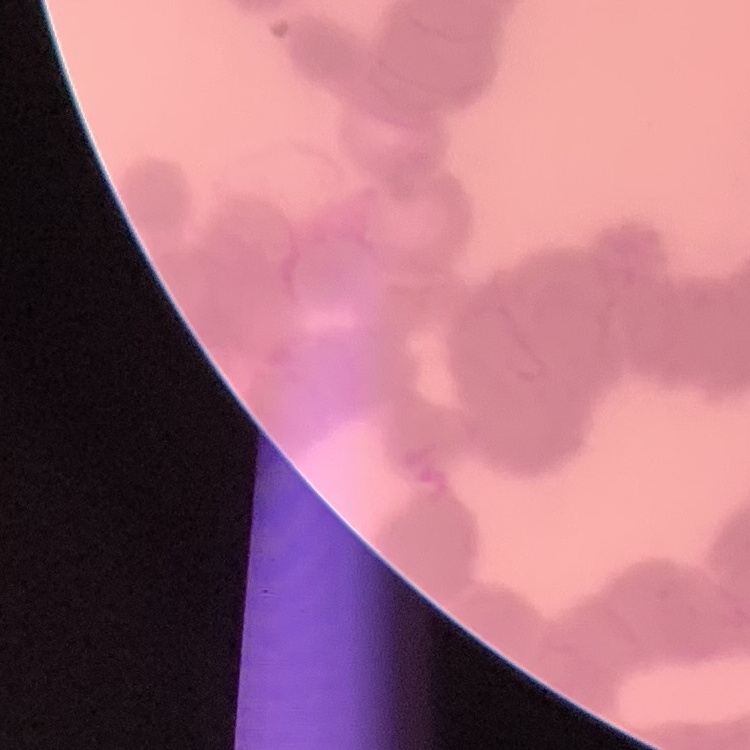

red_blood_cell_morphology: rouleaux formation
image_type: square crop of a larger photomicrograph
stain: Field's or Giemsa
preparation: thin blood smear